Classify this cell by malaria status.
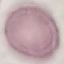

Uninfected.

capture: smartphone camera at the microscope eyepiece
stain: Giemsa
preparation: thin blood smear
image_type: automatically extracted cell patch, resized to 64 × 64 pixels